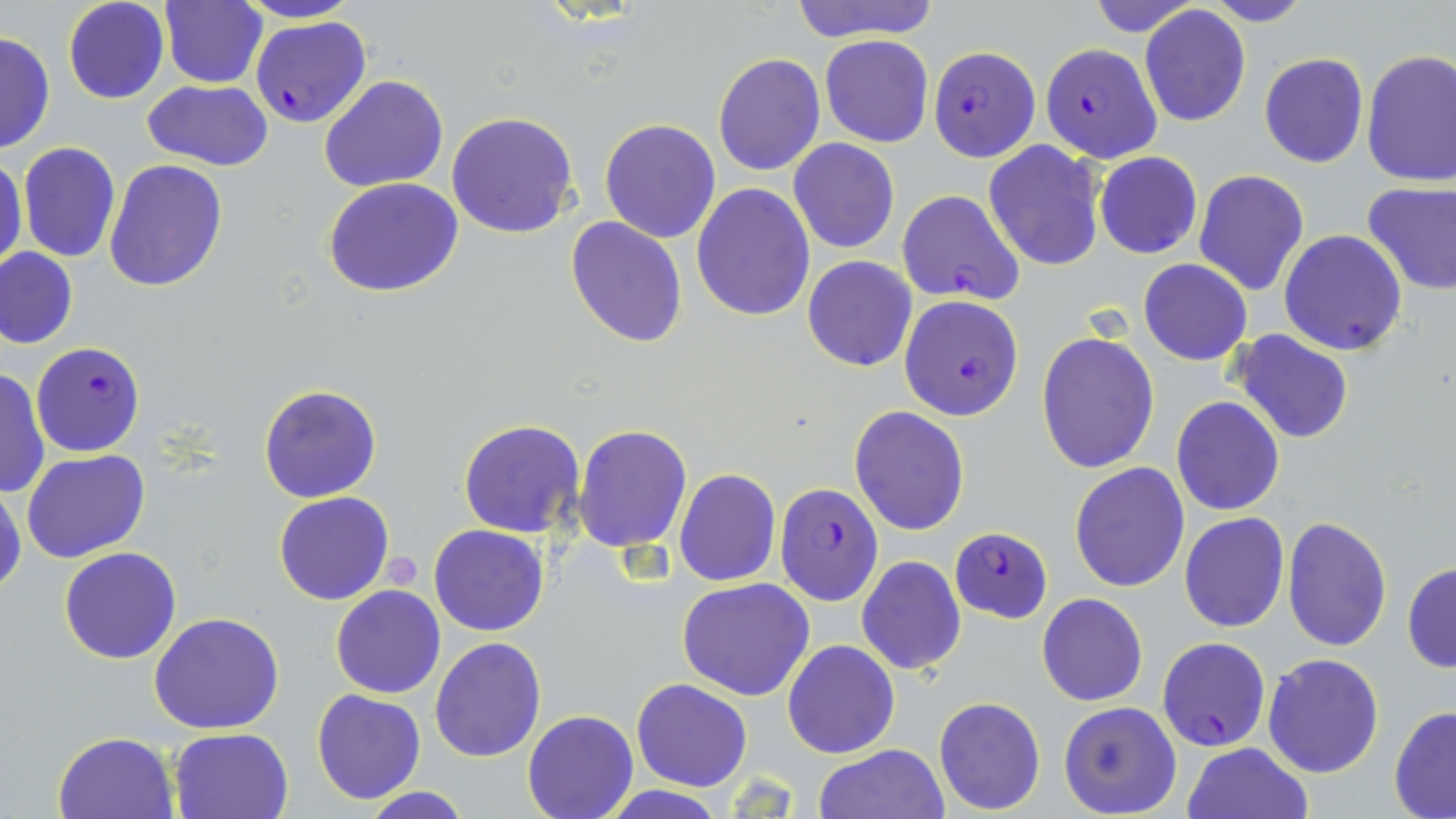

{
  "slide_level_diagnosis": "Plasmodium falciparum",
  "field_of_view": "one of a larger specimen",
  "stain": "May-Grünwald-Giemsa",
  "uninfected_red_blood_cell_locations": "approximate bounding boxes as (x1, y1, x2, y2) in pixels: (62, 0, 169, 104), (159, 0, 268, 89), (236, 0, 359, 25), (789, 0, 938, 44), (1083, 0, 1206, 39), (1202, 0, 1313, 26), (1139, 6, 1252, 127), (0, 32, 55, 154), (820, 36, 934, 148), (1361, 49, 1456, 188), (712, 53, 825, 176), (1258, 53, 1370, 169), (320, 74, 448, 193), (141, 79, 274, 172), (446, 112, 579, 240), (599, 118, 721, 243), (788, 138, 900, 253), (17, 141, 121, 263), (984, 143, 1106, 270), (1093, 151, 1203, 259), (1, 155, 26, 268), (103, 159, 228, 292), (1193, 168, 1309, 295), (323, 178, 464, 297), (1361, 180, 1456, 296), (691, 183, 816, 322), (566, 217, 688, 348), (1279, 229, 1407, 357), (0, 247, 78, 349), (803, 256, 917, 372), (1138, 259, 1252, 366), (1230, 329, 1356, 445), (1036, 331, 1160, 474), (0, 367, 49, 500), (259, 382, 382, 503), (1171, 396, 1284, 516), (849, 405, 969, 536), (458, 418, 584, 537), (571, 423, 693, 553), (23, 449, 149, 563), (1068, 461, 1190, 593), (674, 469, 780, 586), (0, 484, 24, 596), (274, 490, 393, 604), (1180, 512, 1289, 631), (1281, 515, 1392, 652), (430, 524, 548, 636), (58, 547, 181, 664), (857, 556, 967, 674), (1402, 561, 1456, 672), (678, 577, 816, 701), (330, 585, 446, 699), (1037, 593, 1147, 706), (149, 612, 285, 734), (430, 637, 546, 761), (782, 639, 900, 759), (1262, 653, 1384, 776), (631, 677, 753, 793), (311, 689, 426, 804), (933, 696, 1045, 814), (1058, 701, 1182, 817), (1389, 706, 1456, 817), (522, 711, 637, 819), (169, 727, 294, 818), (54, 731, 180, 819), (1182, 742, 1313, 819), (812, 744, 949, 819), (358, 785, 473, 819), (601, 786, 726, 817)",
  "magnification": "1000x",
  "platelet_locations": "approximate bounding boxes as (x1, y1, x2, y2) in pixels: (382, 551, 425, 589)",
  "preparation": "thin blood smear",
  "modality": "optical microscopy",
  "image_size": "1456×819 pixels",
  "plasmodium_falciparum_infected_red_blood_cell_locations": "approximate bounding boxes as (x1, y1, x2, y2) in pixels: (251, 16, 371, 128), (1038, 43, 1163, 161), (928, 46, 1040, 162), (896, 190, 1024, 306), (899, 295, 1024, 420), (31, 341, 147, 457), (774, 482, 884, 606), (951, 525, 1052, 624), (1157, 637, 1270, 751)"
}